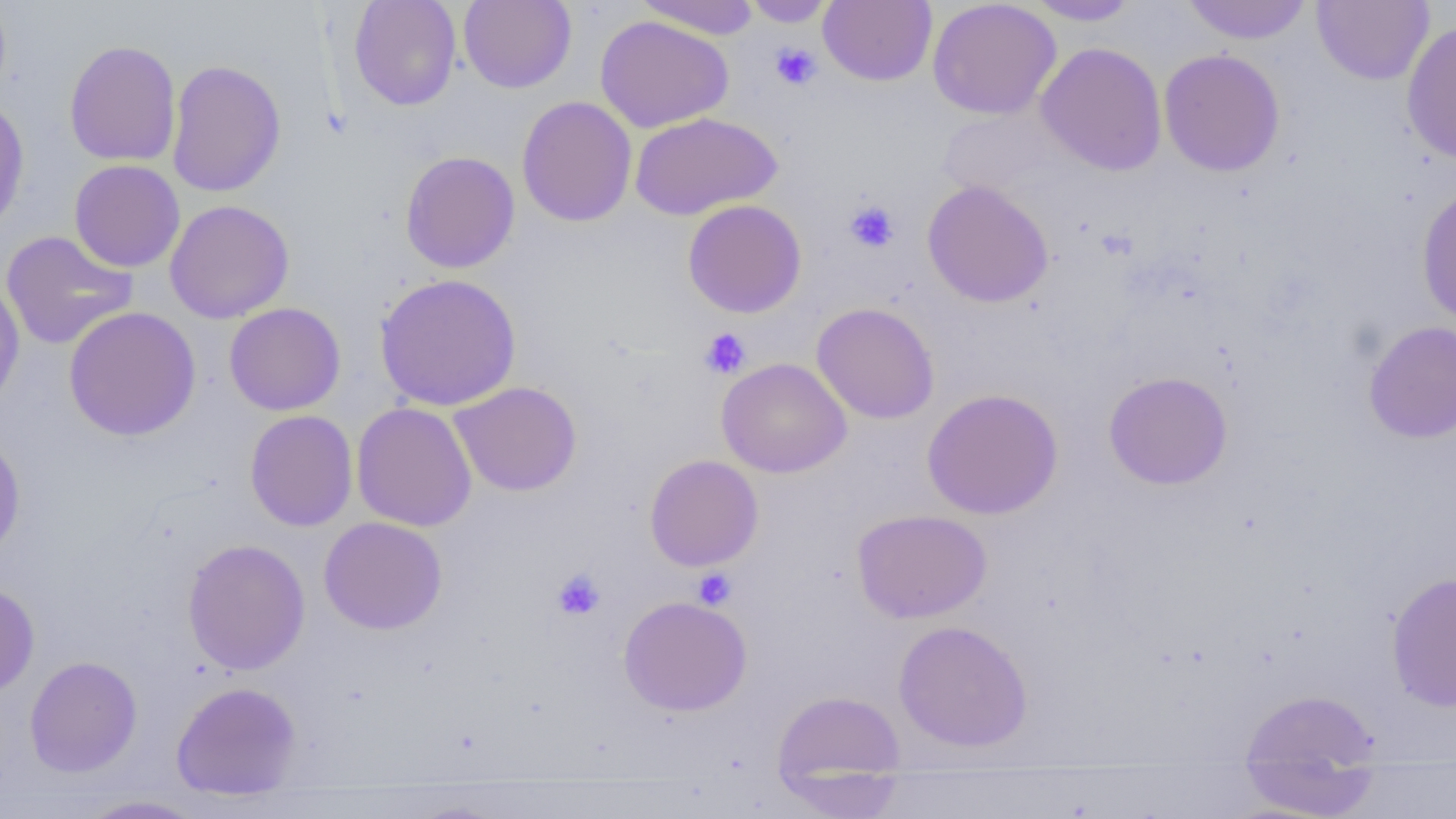

Summary:
  - Coordinate format: approximate bounding boxes as named x1/y1/x2/y2 corners in pixels
  - Platelet locations: (x1=770, y1=42, x2=822, y2=90), (x1=844, y1=199, x2=900, y2=253), (x1=699, y1=328, x2=752, y2=379), (x1=693, y1=567, x2=737, y2=610), (x1=552, y1=568, x2=605, y2=620)
  - Uninfected red blood cell locations: (x1=349, y1=0, x2=462, y2=111), (x1=459, y1=0, x2=576, y2=93), (x1=634, y1=0, x2=761, y2=39), (x1=742, y1=0, x2=836, y2=27), (x1=818, y1=0, x2=936, y2=86), (x1=1023, y1=0, x2=1143, y2=25), (x1=1181, y1=0, x2=1313, y2=44), (x1=927, y1=1, x2=1061, y2=120), (x1=1312, y1=1, x2=1434, y2=85), (x1=595, y1=15, x2=734, y2=133), (x1=1401, y1=19, x2=1456, y2=166), (x1=63, y1=40, x2=181, y2=166), (x1=1035, y1=42, x2=1168, y2=175), (x1=1158, y1=49, x2=1285, y2=177), (x1=166, y1=59, x2=287, y2=197), (x1=516, y1=95, x2=637, y2=227), (x1=0, y1=97, x2=30, y2=235), (x1=935, y1=108, x2=1069, y2=199), (x1=630, y1=112, x2=782, y2=221), (x1=400, y1=150, x2=519, y2=273), (x1=69, y1=159, x2=185, y2=272), (x1=922, y1=180, x2=1054, y2=308), (x1=1416, y1=184, x2=1456, y2=327), (x1=682, y1=199, x2=807, y2=318), (x1=164, y1=200, x2=294, y2=323), (x1=1, y1=230, x2=138, y2=350), (x1=375, y1=273, x2=522, y2=411), (x1=0, y1=278, x2=25, y2=415), (x1=224, y1=302, x2=346, y2=416), (x1=812, y1=302, x2=939, y2=424), (x1=63, y1=306, x2=201, y2=442), (x1=1363, y1=320, x2=1456, y2=444), (x1=717, y1=357, x2=852, y2=478), (x1=1103, y1=371, x2=1233, y2=490), (x1=450, y1=381, x2=582, y2=497), (x1=922, y1=388, x2=1063, y2=519), (x1=351, y1=402, x2=477, y2=532), (x1=244, y1=410, x2=358, y2=532), (x1=0, y1=433, x2=26, y2=562), (x1=644, y1=454, x2=764, y2=571), (x1=852, y1=509, x2=992, y2=623), (x1=318, y1=516, x2=447, y2=635), (x1=183, y1=538, x2=310, y2=675), (x1=1386, y1=570, x2=1456, y2=712), (x1=0, y1=582, x2=40, y2=698), (x1=618, y1=595, x2=753, y2=716), (x1=893, y1=620, x2=1033, y2=752), (x1=24, y1=656, x2=143, y2=777), (x1=171, y1=681, x2=302, y2=799), (x1=1239, y1=689, x2=1380, y2=771), (x1=771, y1=690, x2=906, y2=795), (x1=1237, y1=763, x2=1383, y2=818), (x1=76, y1=794, x2=209, y2=818)
  - Slide-level diagnosis: negative for blood parasites
  - Field of view: single
  - Image size: 1456×819 pixels
  - Magnification: 1000x
  - Modality: light microscopy
  - Preparation: thin blood smear